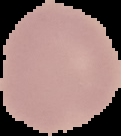
From a thin blood film. Image is 121×136 pixels. Result: no malaria parasites detected. The area outside the segmented cell region is set to black.